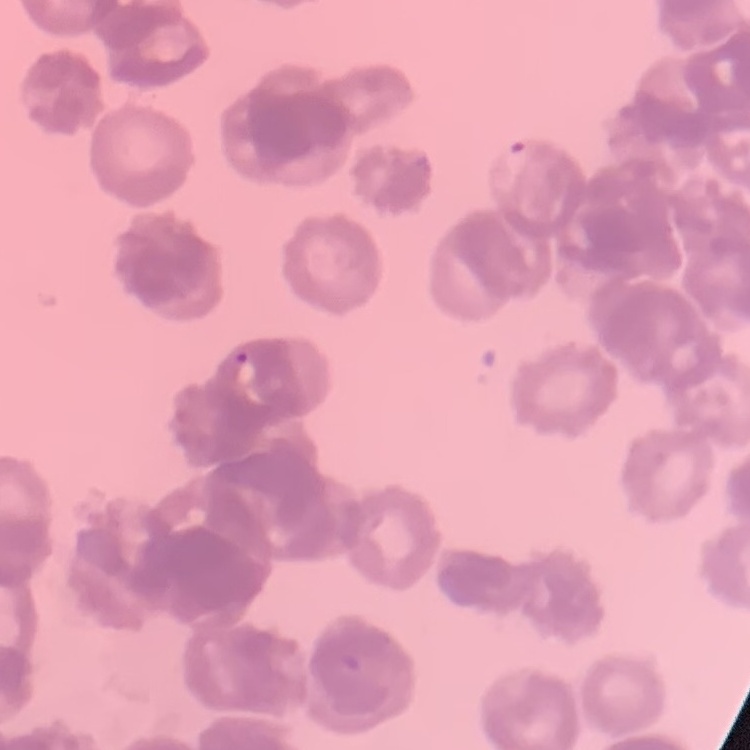
red_blood_cell_morphology: rouleaux formation
image_type: one tile cut from a larger photomicrograph
stain: Field's or Giemsa
preparation: thin blood smear